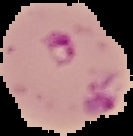
{
  "preparation": "thin blood smear",
  "image_type": "segmented cell region with the area outside set to black",
  "image_size": "133×136 pixels",
  "malaria_status": "parasitized"
}